Assess the morphology of the red blood cells.
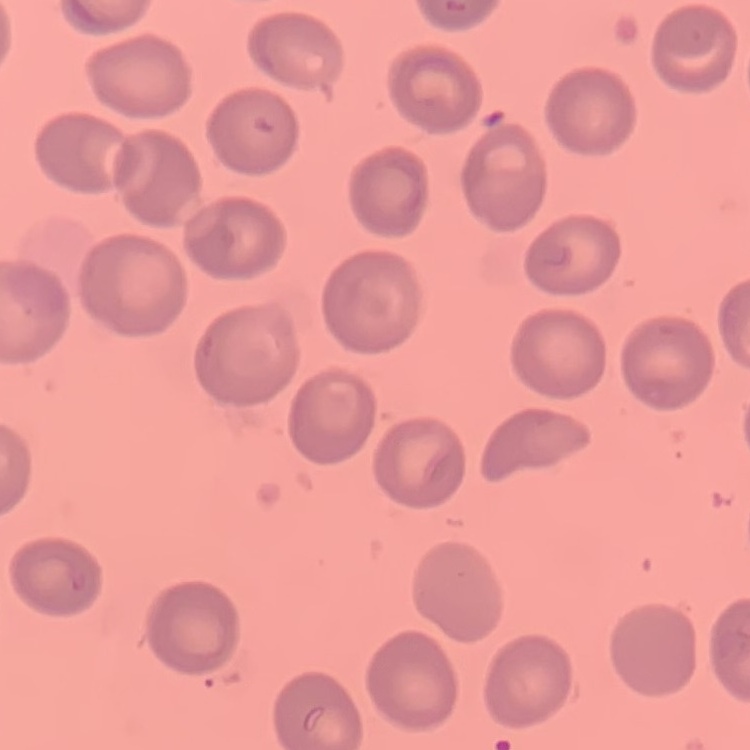
No rouleaux formation.

stain: Field's or Giemsa
image_type: one tile cut from a larger photomicrograph
preparation: thin peripheral smear